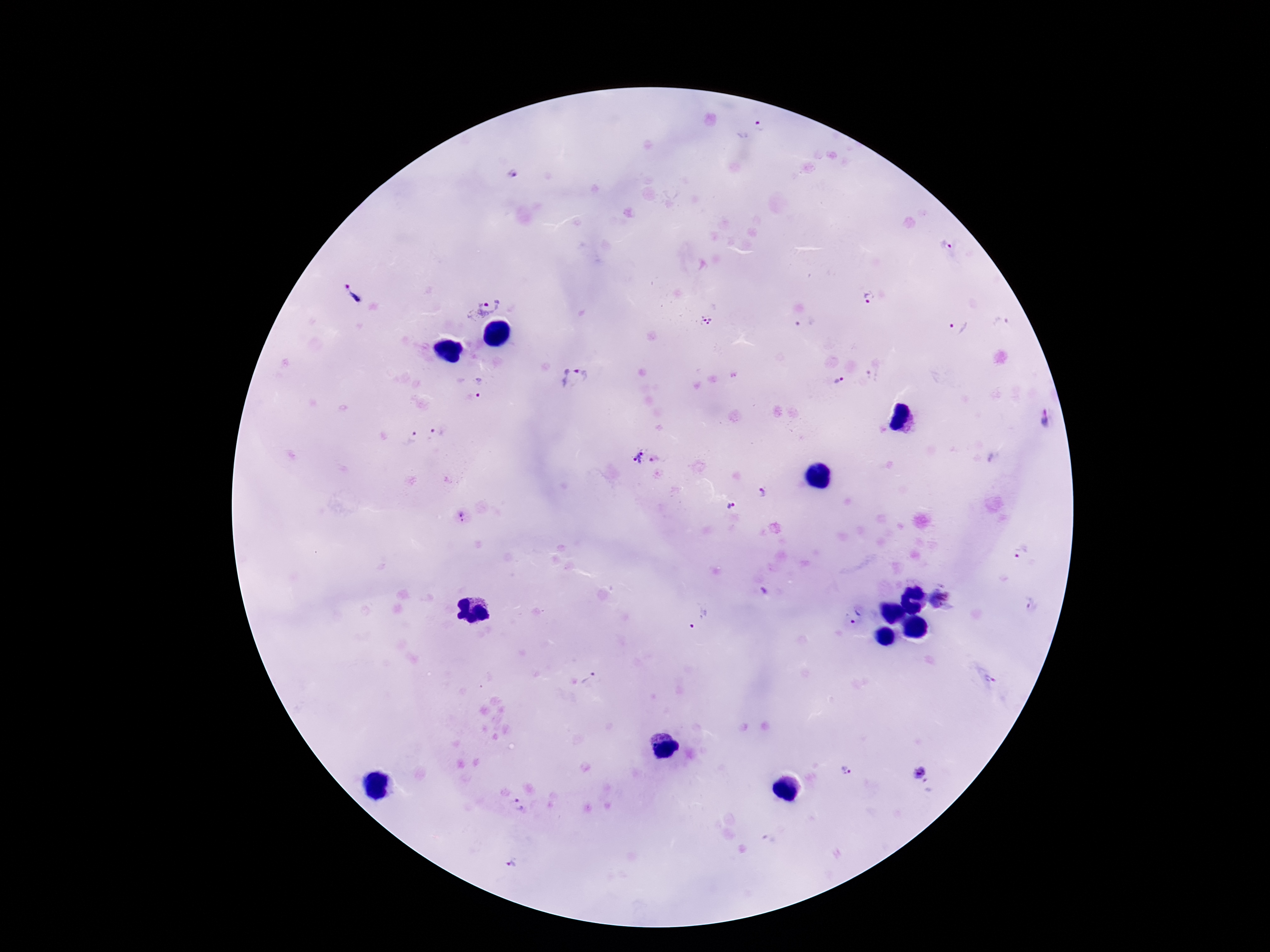
Approximate centers as [x, y] in pixels.
Summary:
  - Plasmodium parasite locations: [750, 129], [516, 176], [355, 292], [870, 298], [481, 301], [707, 322], [1001, 322], [807, 324], [957, 326], [873, 375], [575, 378], [840, 381], [481, 388], [1046, 422], [433, 438], [412, 439], [645, 458], [764, 491], [732, 506], [462, 517], [1022, 552], [762, 592], [941, 597], [1033, 605], [856, 617], [702, 621], [591, 679], [846, 770], [922, 775], [521, 805], [513, 863]
  - Capture: smartphone camera through the microscope eyepiece
  - Magnification: 100x
  - Patient malaria status: infected
  - Preparation: thick peripheral-blood smear
  - Field of view: single
  - Stain: Giemsa
  - Image size: 1270×952 pixels